State which parasite is depicted.
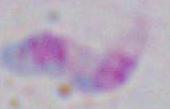

Toxoplasma gondii.

modality = micrograph
magnification = 1000x